Assess the morphology of the red blood cells.
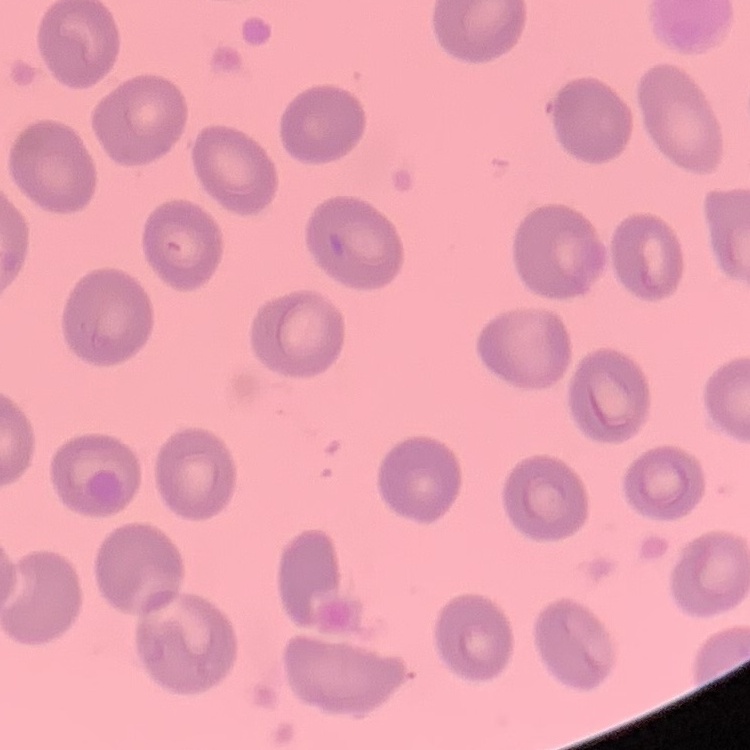

No rouleaux formation.

Thin blood film. Field's or Giemsa stain. Square crop of a larger photomicrograph.